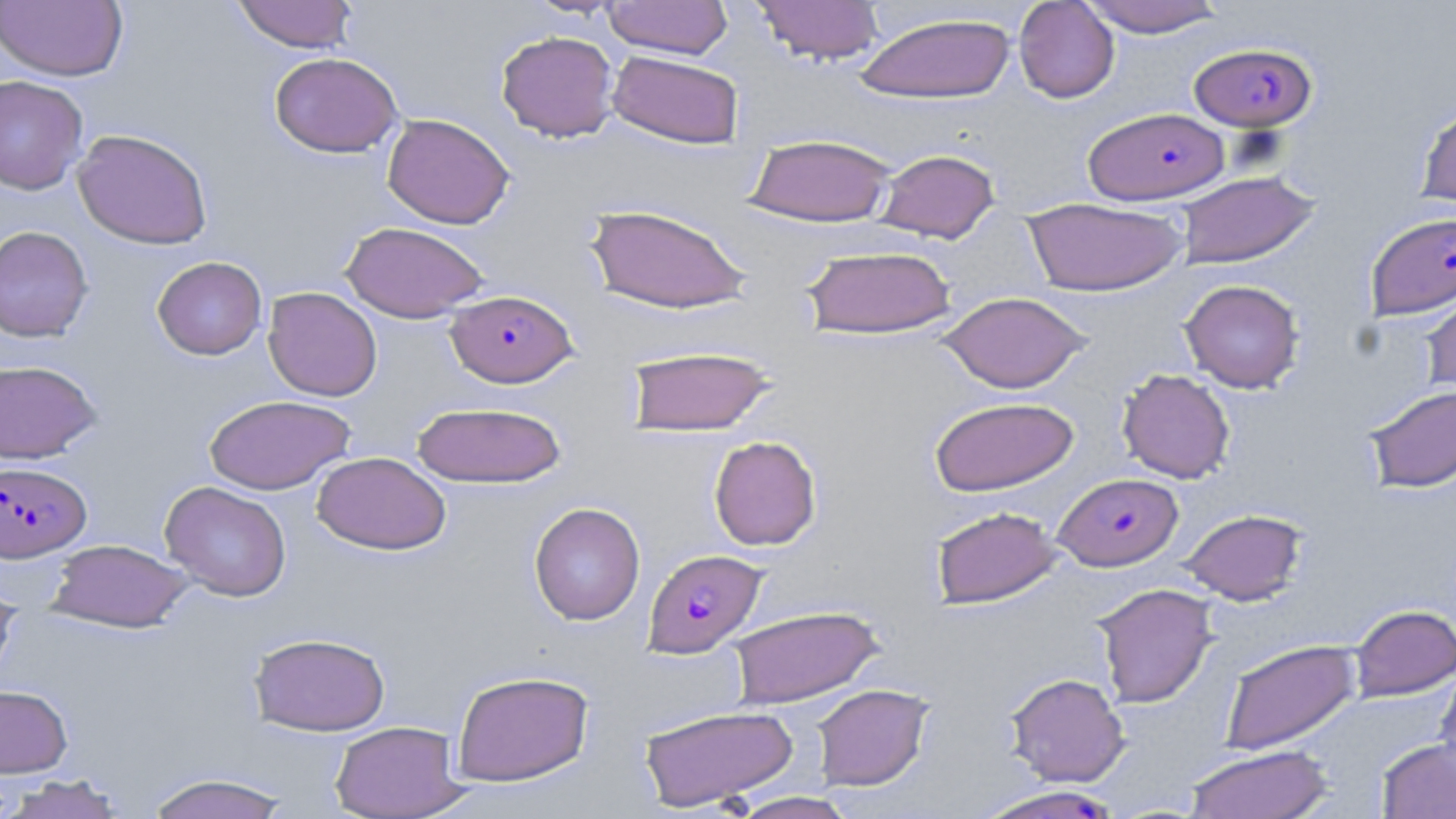

Approximate bounding boxes as [x1, y1, x2, y2] in pixels. Uninfected red blood cell locations: [233, 0, 358, 53], [524, 0, 624, 19], [603, 0, 734, 59], [752, 0, 886, 65], [0, 1, 128, 82], [1014, 1, 1120, 103], [1078, 1, 1226, 37], [855, 12, 1016, 104], [496, 31, 619, 142], [607, 50, 744, 149], [269, 52, 403, 158], [0, 75, 88, 195], [1416, 102, 1456, 212], [382, 113, 515, 229], [72, 129, 212, 249], [744, 133, 895, 227], [875, 148, 1000, 243], [1176, 171, 1321, 269], [1022, 197, 1188, 296], [586, 203, 753, 315], [341, 221, 489, 323], [0, 225, 94, 342], [801, 245, 957, 340], [152, 256, 267, 360], [1419, 278, 1456, 401], [1180, 279, 1305, 393], [263, 286, 383, 401], [937, 291, 1092, 393], [625, 345, 777, 436], [0, 360, 101, 463], [1117, 368, 1235, 483], [1363, 384, 1456, 493], [203, 394, 356, 494], [928, 396, 1079, 496], [412, 401, 567, 488], [709, 435, 822, 551], [312, 451, 450, 555], [159, 481, 292, 601], [529, 502, 646, 625], [930, 506, 1063, 609], [1180, 508, 1308, 604], [47, 539, 192, 632], [1092, 582, 1219, 708], [0, 586, 20, 688], [1349, 604, 1456, 700], [728, 605, 884, 709], [249, 632, 390, 736], [1219, 639, 1360, 755], [1435, 664, 1456, 778], [451, 670, 594, 786], [1005, 672, 1131, 787], [811, 684, 932, 790], [0, 685, 72, 778], [637, 704, 798, 811], [330, 720, 467, 818], [1376, 739, 1456, 818], [1184, 744, 1335, 819], [143, 772, 295, 819], [1, 773, 128, 819], [974, 785, 1126, 819], [727, 792, 860, 819]. Plasmodium falciparum-infected red blood cell locations: [1189, 42, 1316, 131], [1084, 107, 1229, 204], [1364, 211, 1456, 321], [446, 289, 577, 388], [0, 461, 91, 562], [1055, 473, 1182, 571], [643, 548, 766, 657]. Slide-level diagnosis: Plasmodium falciparum. One field of a larger specimen. 1000x magnification. Thin blood film. Image is 1456×819 pixels. Optical microscopy. May-Grünwald-Giemsa-stained preparation.